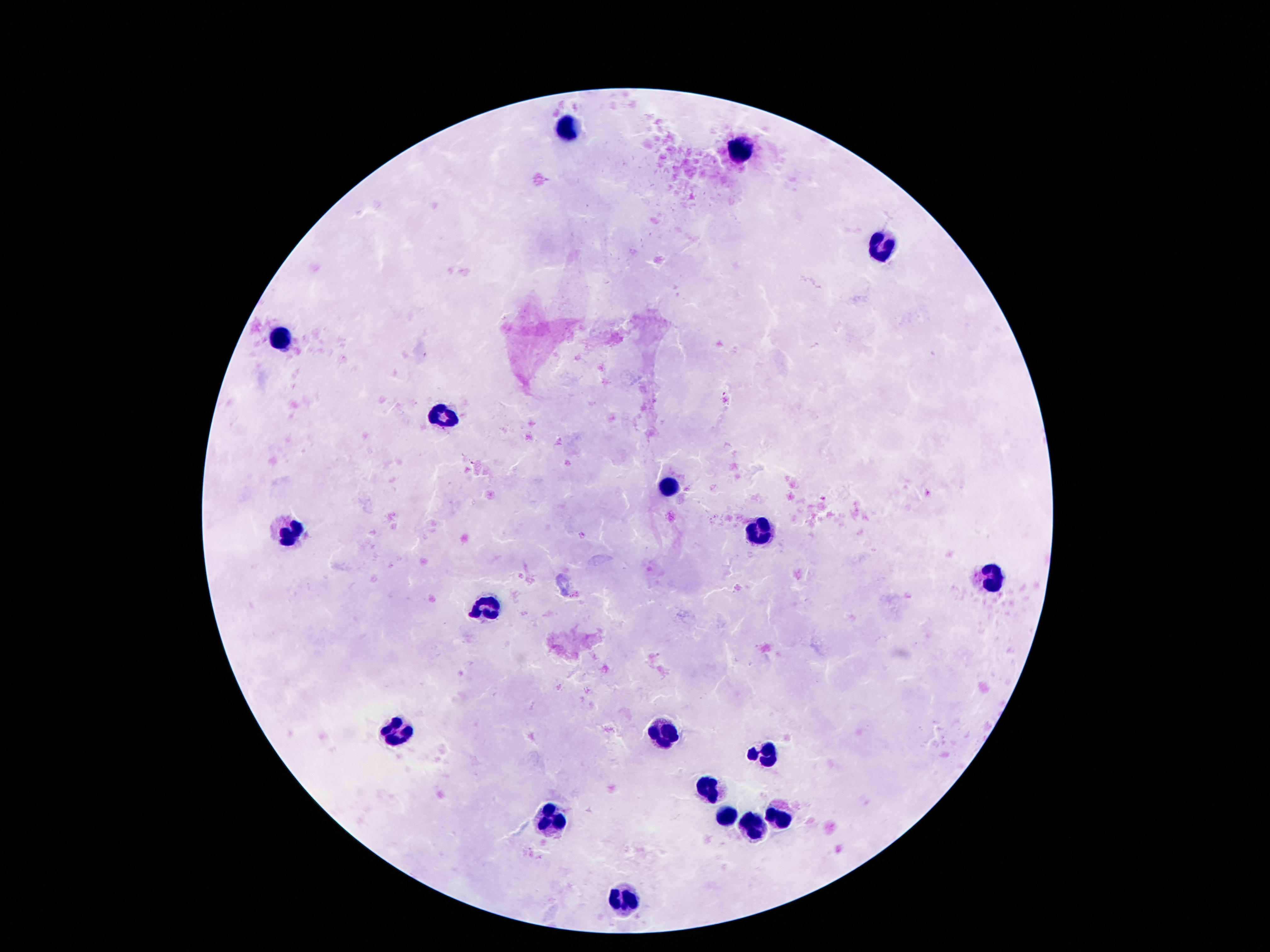
preparation = thick blood film
field of view = one from this slide
stain = Giemsa
image size = 1270×952 pixels
magnification = 100x
patient malaria status = not infected
leukocyte locations = approximate centers as (x, y) in pixels: (571, 130), (739, 147), (888, 247), (282, 337), (443, 417), (667, 487), (757, 530), (290, 533), (993, 577), (487, 609), (671, 728), (398, 732), (767, 755), (710, 793), (724, 816), (548, 822), (780, 822), (749, 828), (624, 900)
capture = smartphone camera through the microscope eyepiece